State which parasite is depicted.
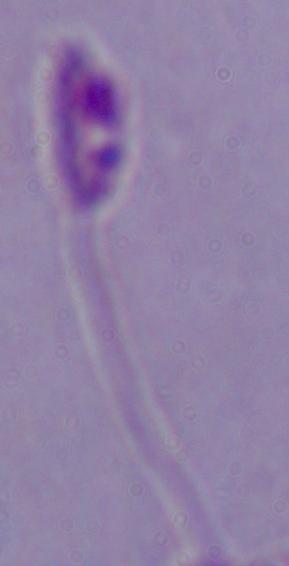
Leishmania.

modality: micrograph
magnification: 1000x